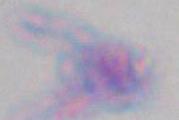

Toxoplasma gondii is seen. Captured at 1000x magnification. Photomicrograph.